State the blood parasite species.
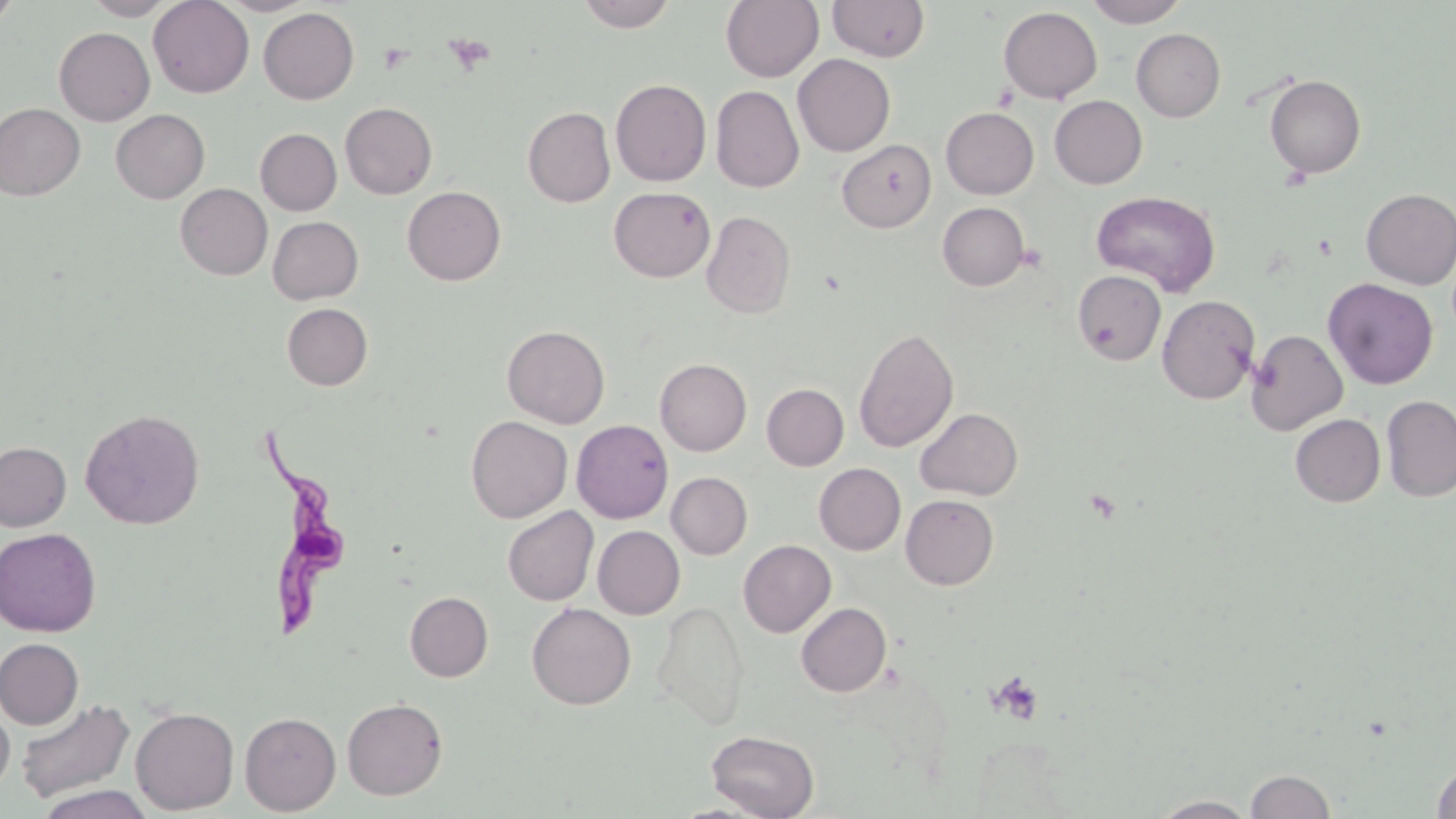
Trypanosoma brucei.

{
  "modality": "optical microscopy",
  "uninfected_red_blood_cell_locations": "approximate bounding boxes as [x1, y1, x2, y2] in pixels: [0, 0, 21, 27], [83, 0, 178, 20], [148, 0, 254, 98], [217, 0, 316, 16], [576, 0, 677, 32], [721, 0, 823, 82], [827, 0, 929, 62], [1084, 0, 1188, 27], [998, 6, 1102, 104], [258, 8, 359, 104], [54, 27, 155, 126], [1131, 28, 1225, 122], [792, 54, 895, 156], [1265, 74, 1366, 178], [610, 79, 711, 186], [711, 85, 804, 193], [1049, 95, 1147, 189], [340, 102, 437, 199], [0, 103, 85, 201], [523, 106, 615, 207], [941, 107, 1038, 198], [111, 109, 209, 203], [255, 128, 341, 215], [837, 139, 936, 232], [175, 183, 272, 280], [402, 186, 506, 285], [608, 186, 715, 282], [1360, 188, 1456, 289], [1092, 190, 1220, 295], [937, 202, 1029, 291], [702, 210, 795, 318], [268, 216, 363, 304], [1072, 270, 1167, 365], [1323, 278, 1438, 389], [1157, 295, 1260, 404], [282, 303, 372, 390], [502, 324, 610, 428], [853, 327, 959, 453], [1246, 329, 1348, 435], [655, 358, 751, 456], [762, 383, 848, 470], [1382, 395, 1456, 502], [80, 408, 205, 529], [916, 408, 1022, 500], [1290, 414, 1386, 507], [466, 415, 572, 522], [571, 419, 673, 523], [0, 442, 71, 531], [814, 463, 905, 554], [666, 472, 752, 559], [901, 494, 999, 589], [503, 506, 598, 605], [592, 525, 684, 619], [0, 528, 102, 637], [738, 540, 836, 637], [404, 591, 493, 681], [651, 599, 749, 730], [527, 602, 636, 709], [796, 602, 891, 696], [1, 639, 84, 729], [14, 697, 135, 805], [342, 698, 448, 800], [0, 701, 15, 798], [130, 706, 240, 814], [239, 711, 341, 815], [706, 730, 819, 818], [1431, 762, 1456, 818], [1246, 770, 1336, 818], [36, 785, 154, 819], [1153, 795, 1257, 818]",
  "preparation": "thin blood film",
  "stain": "May-Grünwald-Giemsa",
  "magnification": "1000x",
  "platelet_locations": "approximate bounding boxes as [x1, y1, x2, y2] in pixels: [445, 34, 495, 75], [378, 43, 413, 73], [986, 671, 1045, 725]",
  "image_size": "1456×819 pixels",
  "trypanosoma_brucei_locations": "approximate bounding boxes as [x1, y1, x2, y2] in pixels: [259, 428, 362, 640]",
  "field_of_view": "one of a larger specimen"
}